Identify the cell.
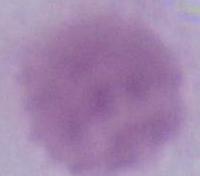
An erythrocyte.

Photomicrograph. 1000x magnification.